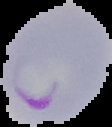
Summary:
  - Result: Plasmodium parasites identified
  - Image size: 112×127 pixels
  - Image type: segmented cell region on a black background
  - Preparation: thin blood film